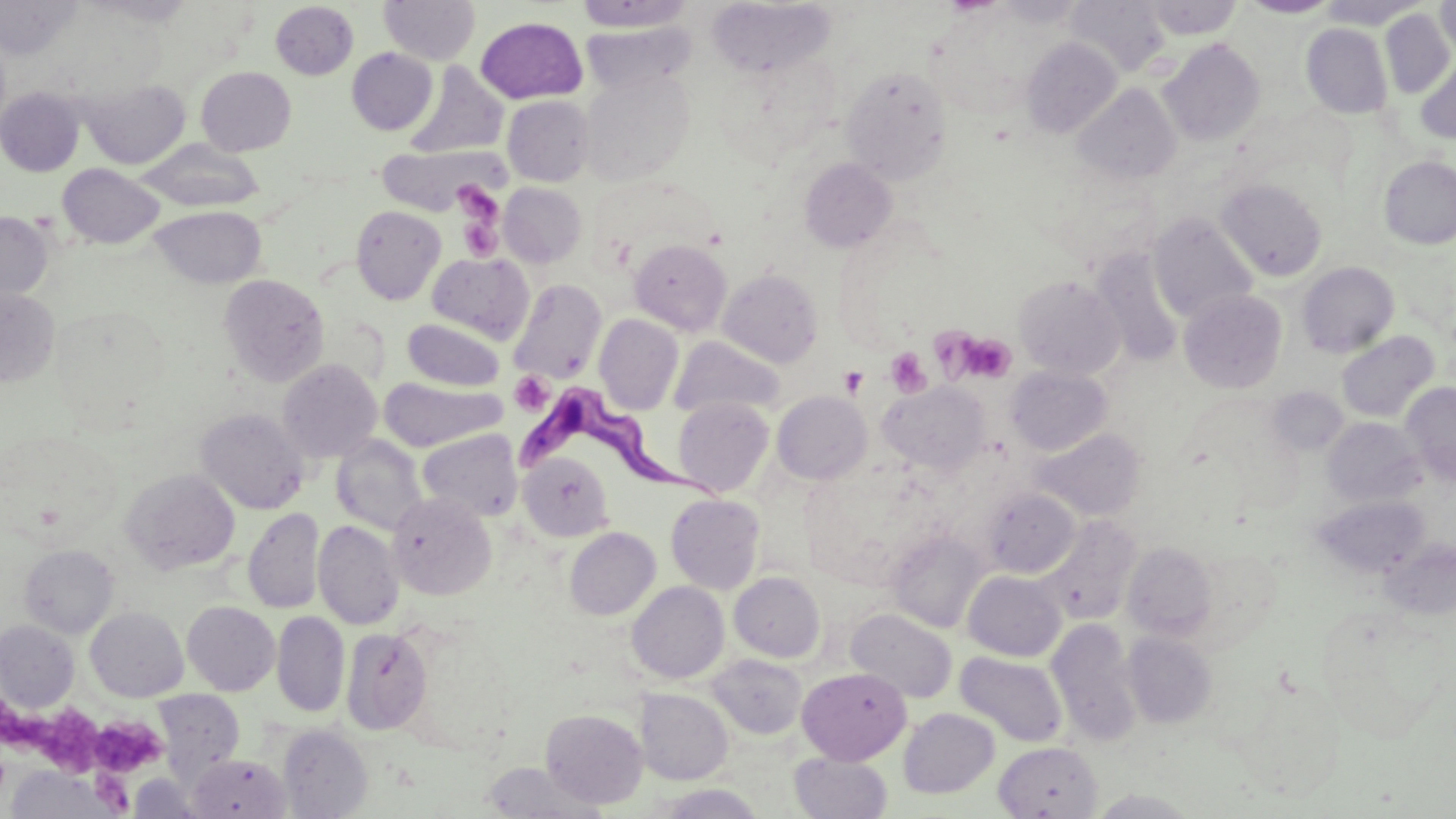 Approximate bounding boxes as (x1, y1, x2, y2) in pixels. Uninfected red blood cell locations: (0, 0, 82, 59), (86, 0, 195, 27), (378, 0, 480, 65), (1066, 0, 1170, 77), (1143, 0, 1242, 39), (1239, 0, 1339, 19), (1318, 0, 1425, 29), (1435, 0, 1456, 59), (573, 1, 696, 32), (708, 1, 835, 79), (270, 2, 358, 80), (1381, 9, 1454, 98), (475, 17, 588, 104), (580, 21, 696, 94), (1301, 23, 1392, 119), (1021, 37, 1122, 138), (1158, 39, 1265, 146), (347, 48, 437, 135), (1416, 57, 1456, 144), (406, 62, 509, 158), (196, 66, 296, 156), (841, 66, 952, 183), (580, 69, 694, 186), (78, 78, 190, 169), (1073, 84, 1181, 185), (0, 88, 84, 176), (502, 95, 594, 186), (136, 139, 265, 212), (377, 143, 501, 216), (1378, 156, 1456, 249), (800, 157, 897, 252), (57, 163, 164, 249), (1216, 178, 1327, 281), (499, 183, 587, 267), (150, 205, 266, 288), (351, 205, 446, 304), (0, 211, 53, 306), (1149, 212, 1258, 325), (630, 238, 732, 335), (1090, 248, 1185, 367), (427, 252, 534, 344), (1297, 261, 1399, 358), (718, 269, 823, 367), (219, 273, 330, 386), (1013, 275, 1125, 379), (508, 278, 606, 384), (0, 288, 60, 387), (1179, 290, 1287, 393), (594, 314, 683, 415), (402, 318, 505, 391), (1336, 331, 1439, 422), (669, 337, 785, 418), (277, 359, 382, 463), (1006, 366, 1112, 456), (380, 378, 505, 451), (879, 382, 990, 475), (1401, 382, 1456, 486), (772, 391, 872, 485), (673, 397, 774, 496), (195, 408, 309, 514), (1323, 418, 1425, 506), (417, 428, 523, 522), (1032, 429, 1146, 520), (1, 431, 120, 542), (331, 435, 428, 536), (519, 452, 614, 541), (121, 469, 240, 574), (980, 489, 1081, 578), (388, 493, 496, 599), (666, 493, 765, 594), (1314, 495, 1429, 579), (243, 508, 324, 614), (1041, 515, 1141, 623), (313, 520, 404, 630), (564, 527, 660, 620), (888, 530, 989, 633), (1381, 538, 1456, 620), (1123, 542, 1218, 641), (19, 544, 120, 638), (963, 570, 1066, 661), (729, 571, 825, 662), (627, 581, 729, 684), (182, 602, 280, 695), (86, 607, 188, 701), (846, 609, 957, 703), (272, 612, 349, 717), (0, 620, 79, 712), (1046, 621, 1141, 744), (341, 627, 433, 735), (1123, 631, 1217, 727), (955, 651, 1068, 747), (706, 654, 807, 739), (797, 666, 911, 765), (635, 688, 733, 785), (152, 690, 245, 779), (899, 707, 1000, 798), (541, 709, 648, 809), (277, 724, 372, 818), (994, 741, 1102, 818), (790, 751, 892, 819), (188, 754, 290, 819), (479, 763, 606, 818), (4, 766, 123, 818), (127, 773, 204, 818), (654, 784, 767, 819). Platelet locations: (453, 182, 506, 261), (958, 332, 1017, 382), (885, 347, 931, 398), (839, 366, 868, 397), (509, 372, 553, 416), (1, 696, 111, 776), (88, 716, 167, 777). Trypanosoma brucei locations: (515, 384, 725, 506). Slide-level diagnosis: Trypanosoma brucei. Single field of view. Light microscopy. Captured at 1000x magnification. Thin blood film. May-Grünwald-Giemsa stain. Image is 1456×819 pixels.